Outline each Plasmodium falciparum-infected red blood cell.
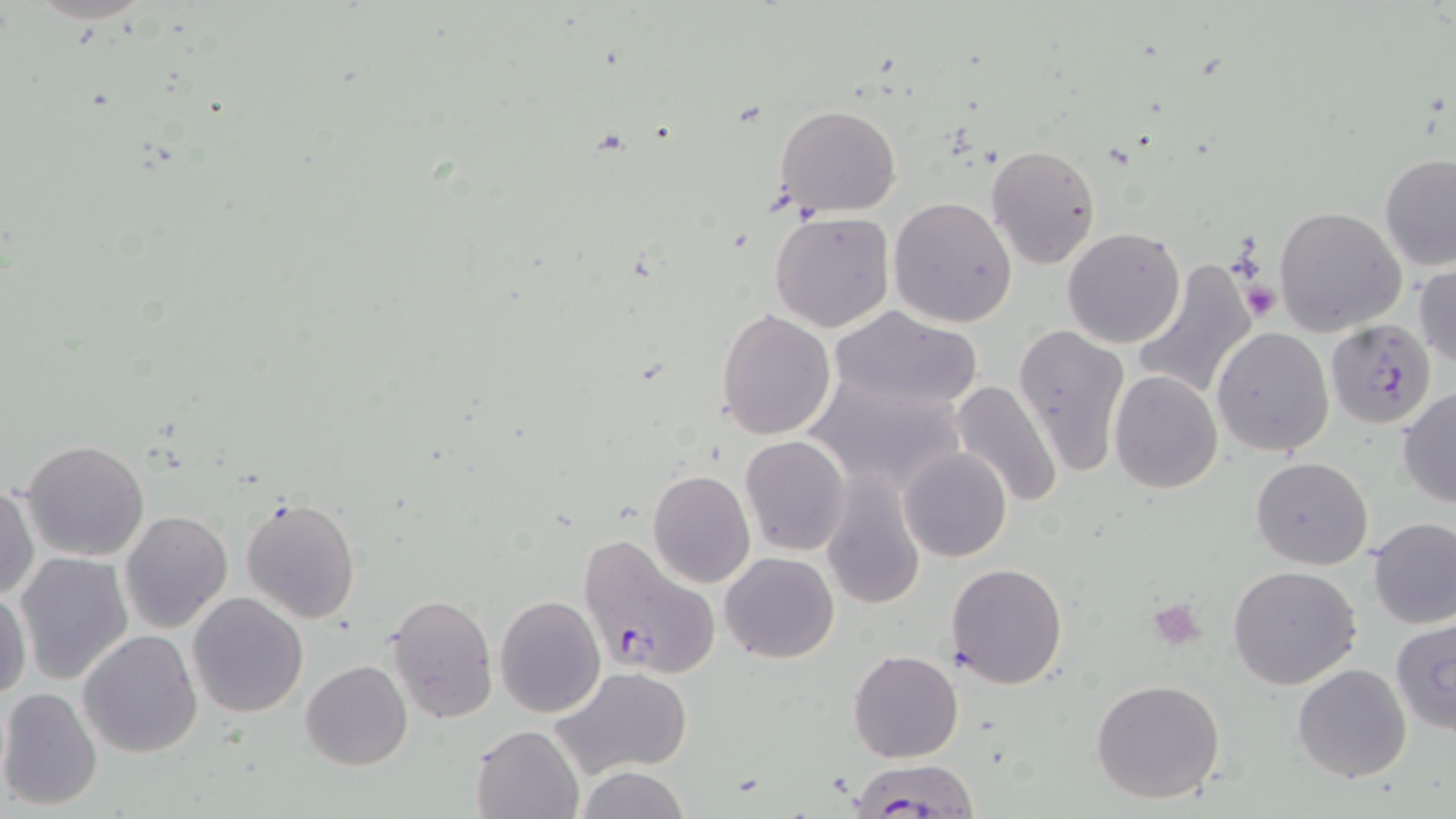

Approximate bounding boxes as (x1, y1, x2, y2) in pixels.
Plasmodium falciparum-infected red blood cells: (1327, 322, 1437, 430), (576, 531, 722, 680), (847, 758, 982, 816).

Summary:
  - Platelet locations: (1242, 283, 1279, 320), (1147, 598, 1207, 650)
  - Uninfected red blood cell locations: (775, 105, 903, 216), (985, 145, 1100, 268), (1378, 153, 1456, 271), (888, 196, 1018, 326), (1274, 206, 1408, 337), (768, 209, 896, 334), (1062, 226, 1186, 348), (1130, 257, 1260, 403), (1413, 262, 1456, 371), (828, 306, 984, 414), (715, 309, 837, 440), (1012, 323, 1130, 480), (1211, 327, 1335, 457), (1110, 369, 1223, 494), (806, 371, 967, 494), (949, 380, 1063, 508), (1397, 388, 1456, 508), (739, 435, 851, 556), (21, 439, 150, 562), (899, 448, 1011, 563), (1251, 457, 1373, 570), (819, 468, 927, 609), (647, 469, 755, 587), (1, 483, 39, 603), (240, 496, 362, 624), (119, 509, 233, 632), (1367, 516, 1456, 629), (15, 551, 134, 685), (719, 552, 839, 662), (945, 562, 1068, 688), (1227, 565, 1362, 688), (0, 587, 30, 698), (187, 592, 309, 717), (386, 592, 497, 725), (494, 593, 605, 718), (1390, 620, 1456, 734), (78, 630, 203, 757), (848, 650, 963, 763), (300, 659, 414, 770), (1293, 664, 1410, 783), (551, 665, 695, 779), (1090, 679, 1227, 805), (0, 686, 103, 812), (470, 725, 584, 819), (574, 765, 691, 819)
  - Slide-level diagnosis: Plasmodium falciparum
  - Magnification: 1000x
  - Preparation: thin blood smear
  - Modality: optical microscopy
  - Stain: May-Grünwald-Giemsa
  - Field of view: one of a larger specimen
  - Image size: 1456×819 pixels